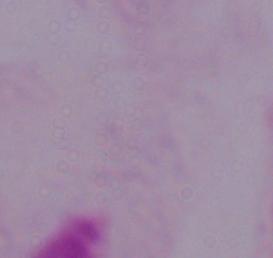
identification = trichomonad
modality = micrograph
magnification = 1000x